Assess this cell for malaria.
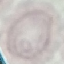
Uninfected.

stain = Giemsa
capture = smartphone through the microscope eyepiece
image type = automatically extracted cell patch, resized to 64 × 64 pixels
preparation = thin blood smear